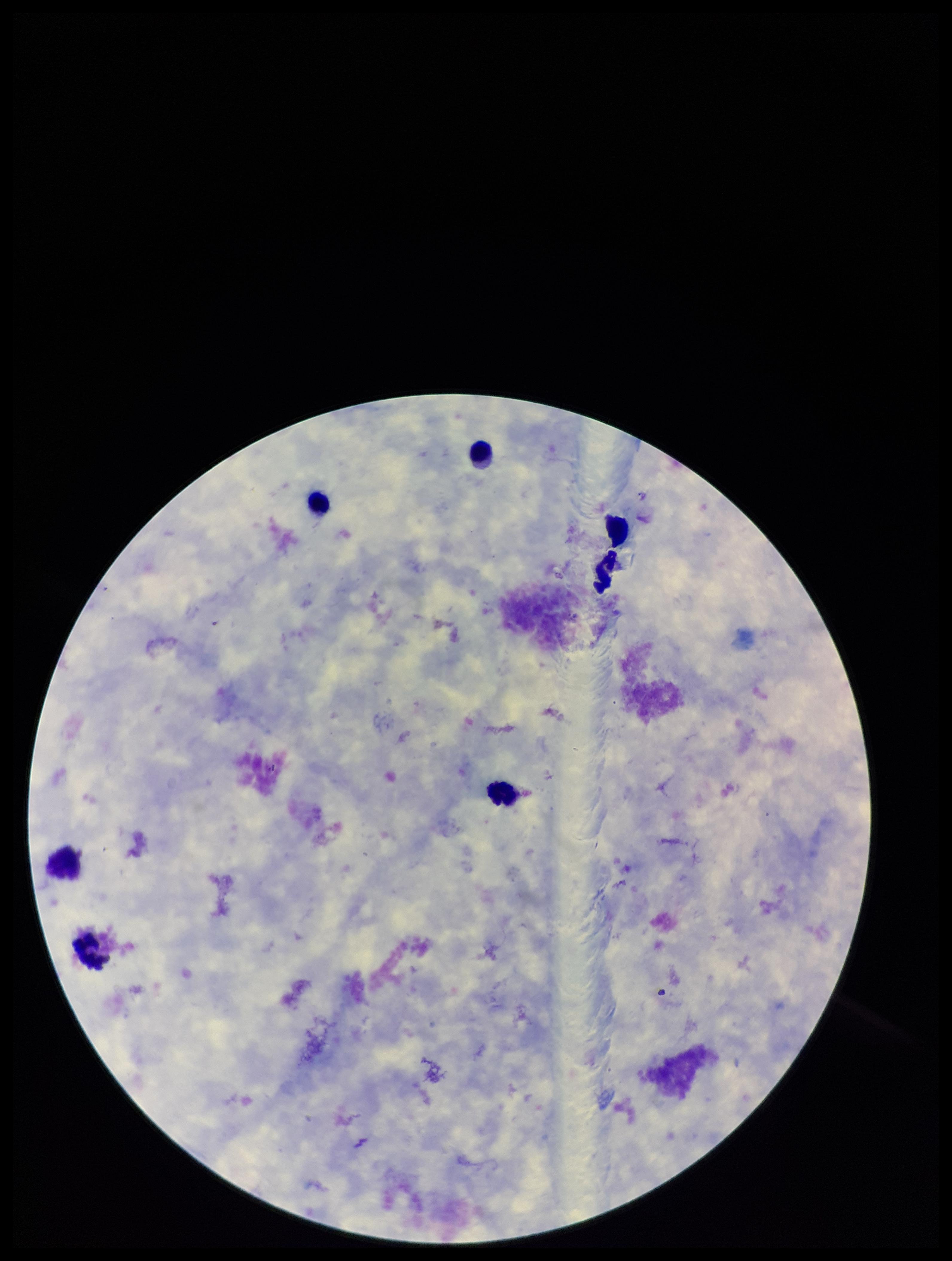
Plasmodium parasites: none seen. Image is 952×1261 pixels. Parasite count: 0. Patient malaria status: negative. Photographed through the microscope eyepiece with a smartphone camera. Giemsa stain. Preparation: thick. One field from this slide. Leukocyte count: 6.